Outline each Plasmodium falciparum-infected red blood cell.
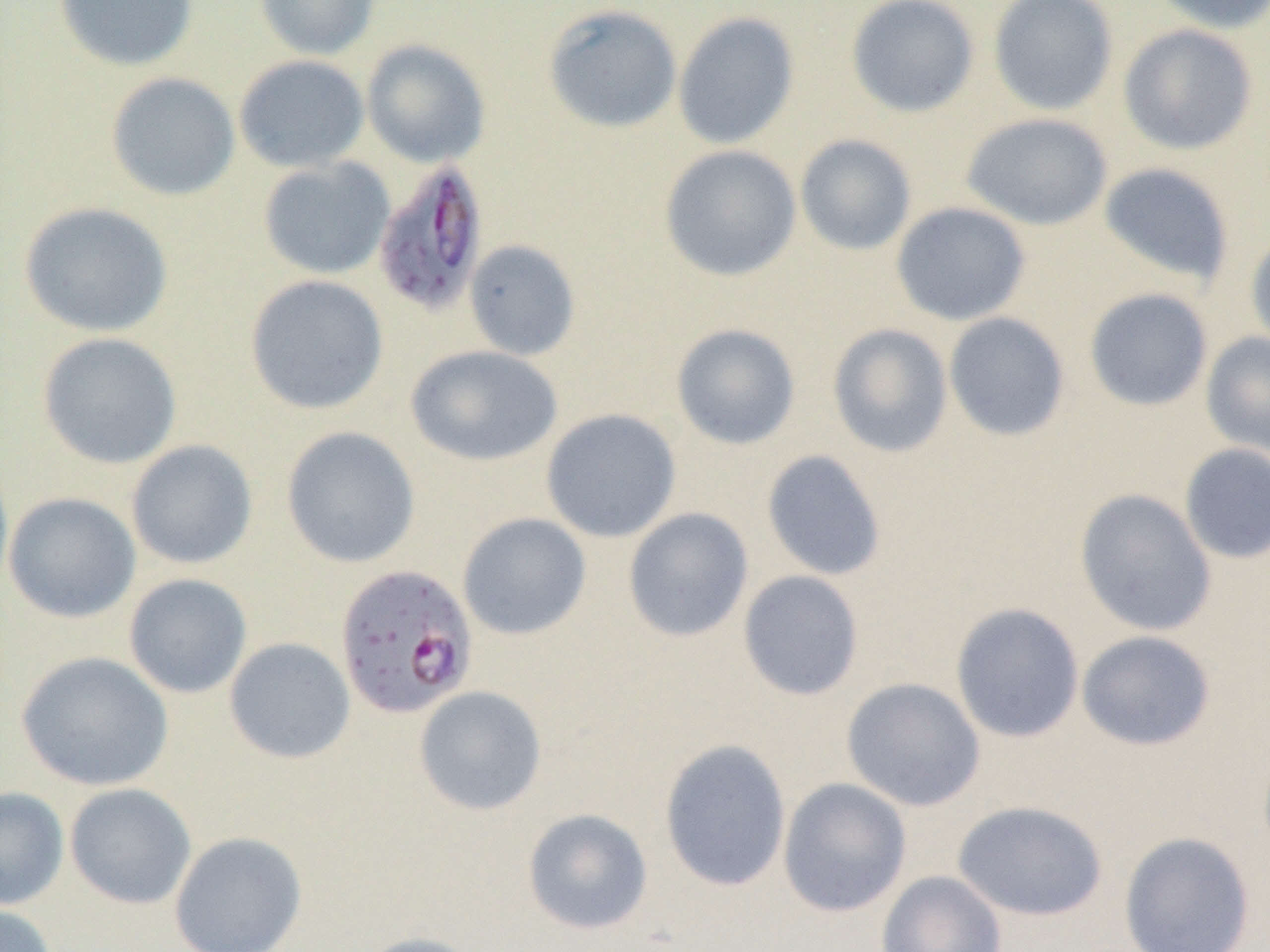
Approximate bounding boxes as (x1,y1)-(x2,y2) corner pairs in pixels.
Plasmodium falciparum-infected red blood cells: (372,160)-(489,316), (337,561)-(482,715).

Uninfected red blood cell locations: (53,0)-(199,72), (254,0)-(379,61), (845,0)-(979,118), (987,0)-(1119,116), (1148,0)-(1270,34), (542,3)-(682,134), (673,11)-(800,150), (1118,23)-(1258,156), (361,39)-(491,168), (233,55)-(370,173), (105,72)-(240,202), (961,112)-(1113,231), (794,134)-(917,256), (659,145)-(801,281), (258,157)-(395,280), (1098,162)-(1235,286), (18,201)-(173,337), (891,201)-(1031,326), (1246,230)-(1270,353), (464,239)-(581,360), (245,274)-(389,415), (1083,288)-(1214,412), (943,312)-(1070,442), (670,323)-(801,449), (827,323)-(953,458), (37,332)-(183,469), (1201,332)-(1270,459), (405,345)-(562,466), (540,408)-(682,542), (281,426)-(420,568), (126,440)-(258,570), (1179,443)-(1270,565), (761,449)-(887,581), (0,453)-(14,601), (1074,488)-(1217,637), (3,491)-(141,623), (622,507)-(754,642), (457,512)-(592,640), (737,570)-(865,701), (123,573)-(253,699), (950,602)-(1084,743), (1076,630)-(1216,751), (224,637)-(356,764), (15,650)-(174,792), (841,677)-(985,812), (413,686)-(547,816), (659,738)-(792,891), (778,777)-(912,916), (65,782)-(197,909), (0,786)-(69,910), (952,800)-(1108,921), (522,808)-(653,935), (169,831)-(308,952), (1118,831)-(1256,952), (876,871)-(1007,952), (0,903)-(58,952), (351,932)-(486,952). Slide-level diagnosis: Plasmodium falciparum. Optical microscopy. Image is 1270×952 pixels. Captured at 1000x magnification. One field of a larger specimen. Thin blood smear.